Locate every Plasmodium vivax-infected red blood cell.
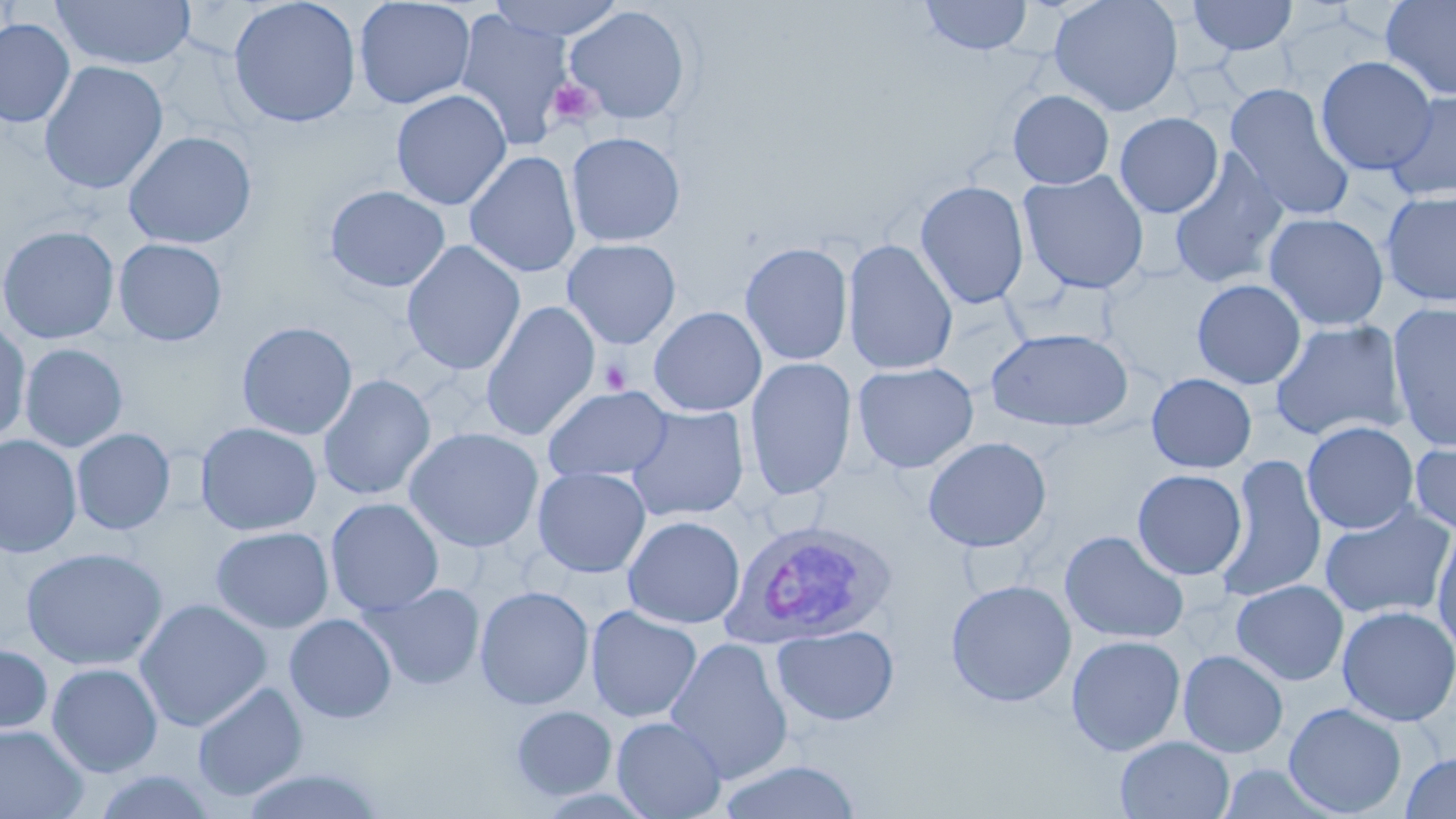

Approximate bounding boxes as (x1,y1)-(x2,y2) corner pairs in pixels.
Plasmodium vivax-infected red blood cells: (720,518)-(894,649).

Summary:
  - Platelet locations: (547,77)-(601,130), (599,359)-(632,394)
  - Uninfected red blood cell locations: (51,0)-(196,71), (227,0)-(362,127), (353,0)-(476,109), (485,0)-(628,41), (919,0)-(1034,56), (1048,0)-(1183,117), (1186,0)-(1299,56), (1379,0)-(1456,101), (564,5)-(693,126), (454,11)-(572,149), (0,18)-(75,127), (1315,56)-(1437,176), (38,61)-(169,195), (1224,84)-(1355,222), (1384,89)-(1456,204), (390,90)-(512,210), (1008,90)-(1114,189), (1114,112)-(1223,218), (123,130)-(257,249), (565,131)-(686,247), (1169,150)-(1290,290), (464,151)-(581,277), (1018,170)-(1150,295), (914,179)-(1030,310), (324,185)-(451,292), (1380,189)-(1456,307), (1263,212)-(1389,332), (0,225)-(120,344), (114,238)-(227,346), (562,238)-(681,349), (842,238)-(959,376), (401,241)-(525,375), (739,241)-(854,365), (1192,279)-(1306,389), (481,301)-(600,442), (1386,302)-(1456,453), (648,306)-(767,416), (0,318)-(31,447), (1269,320)-(1407,442), (236,321)-(358,440), (986,327)-(1135,432), (20,344)-(128,453), (745,357)-(857,500), (852,361)-(979,474), (1146,372)-(1256,473), (318,374)-(435,501), (542,385)-(673,482), (626,406)-(750,522), (1301,421)-(1419,534), (195,422)-(322,536), (404,426)-(544,553), (72,428)-(176,535), (0,434)-(82,558), (1409,435)-(1456,537), (922,436)-(1052,553), (1215,454)-(1327,604), (532,467)-(651,577), (1132,469)-(1247,581), (325,498)-(444,616), (1318,503)-(1455,621), (623,515)-(745,629), (1431,523)-(1456,655), (211,526)-(333,633), (1059,530)-(1190,645), (20,547)-(167,670), (945,579)-(1077,708), (1231,580)-(1349,686), (361,583)-(485,690), (475,585)-(594,710), (135,598)-(272,732), (585,605)-(702,723), (1337,605)-(1456,727), (284,613)-(397,723), (772,624)-(899,727), (1066,634)-(1186,756), (665,636)-(793,785), (0,643)-(52,737), (1178,650)-(1289,758), (46,663)-(163,777), (192,681)-(308,802), (1283,702)-(1407,817), (510,704)-(618,801), (611,716)-(727,819), (0,725)-(89,818), (1115,736)-(1235,819), (1400,751)-(1456,818), (715,760)-(863,818), (237,768)-(389,819), (89,769)-(217,818)
  - Slide-level diagnosis: Plasmodium vivax
  - Field of view: one of a larger specimen
  - Modality: optical microscopy
  - Image size: 1456×819 pixels
  - Preparation: thin blood smear
  - Magnification: 1000x
  - Stain: May-Grünwald-Giemsa